State which parasite is depicted.
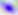
This is Toxoplasma gondii.

Summary:
  - Magnification: 400x
  - Modality: micrograph